Comment on the morphology of the erythrocytes.
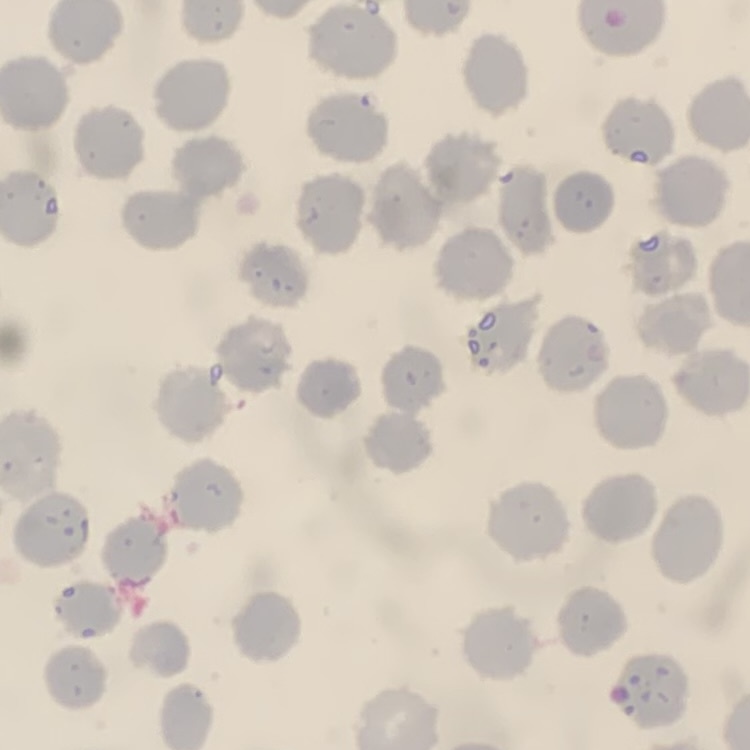

No rouleaux formation.

Summary:
  - Image type: one tile cut from a larger photomicrograph
  - Preparation: thin blood film
  - Stain: Field's or Giemsa